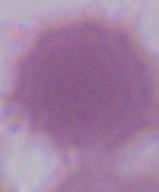
magnification = 1000x
identification = red blood cell
modality = micrograph